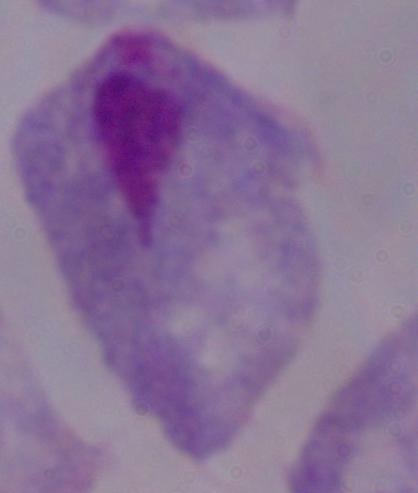
Micrograph. A trichomonad is shown. Captured at 1000x magnification.